Assess the morphology of the erythrocytes.
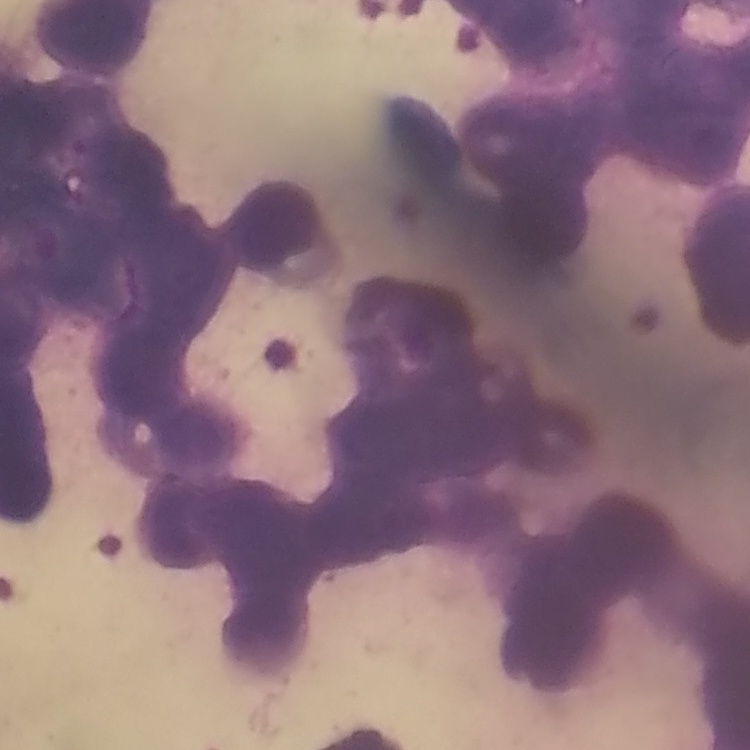
They show rouleaux formation.

One tile cut from a larger photomicrograph. Field's or Giemsa stain. Thin peripheral smear.